Report the malaria status of this cell.
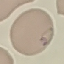
Parasitized.

capture: smartphone through the microscope eyepiece
stain: Giemsa
image_type: cell patch, automatically extracted from a larger field of view and resized to 64 × 64 pixels
preparation: thin blood film